Classify this cell by malaria status.
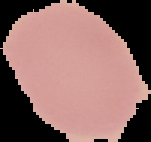
Uninfected.

Cell region segmented out of the field of view; the surrounding area is masked to black. From a thin blood smear. Image is 151×142 pixels.